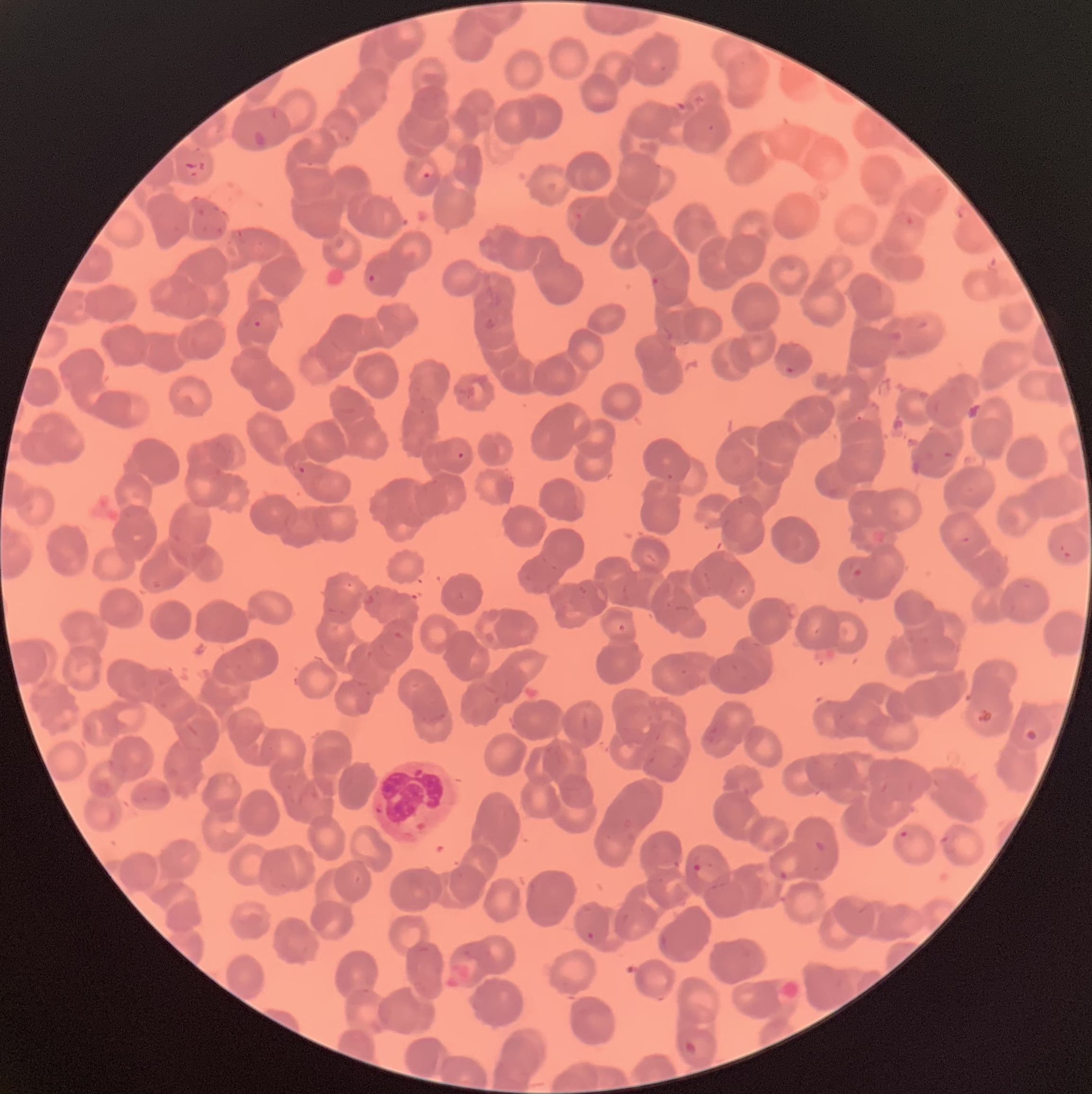
Summary:
  - Coordinate format: approximate bounding boxes as (x1,y1)-(x2,y2) corner pairs in pixels
  - Plasmodium parasite locations: (421,171)-(432,181), (366,273)-(378,283), (651,274)-(659,286), (253,320)-(262,329), (783,364)-(795,376), (456,451)-(465,460), (297,466)-(306,476), (1059,544)-(1073,560), (899,830)-(910,840), (692,853)-(703,872), (779,869)-(789,880), (585,930)-(596,944)
  - Red blood cell morphology: rouleaux formation
  - Image size: 1092×1094 pixels
  - Modality: optical microscopy
  - Preparation: thin blood film